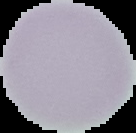
Image is 136×133 pixels. Cell region segmented out of the field of view; the surrounding area is masked to black. Malaria status: uninfected. From a thin blood film.